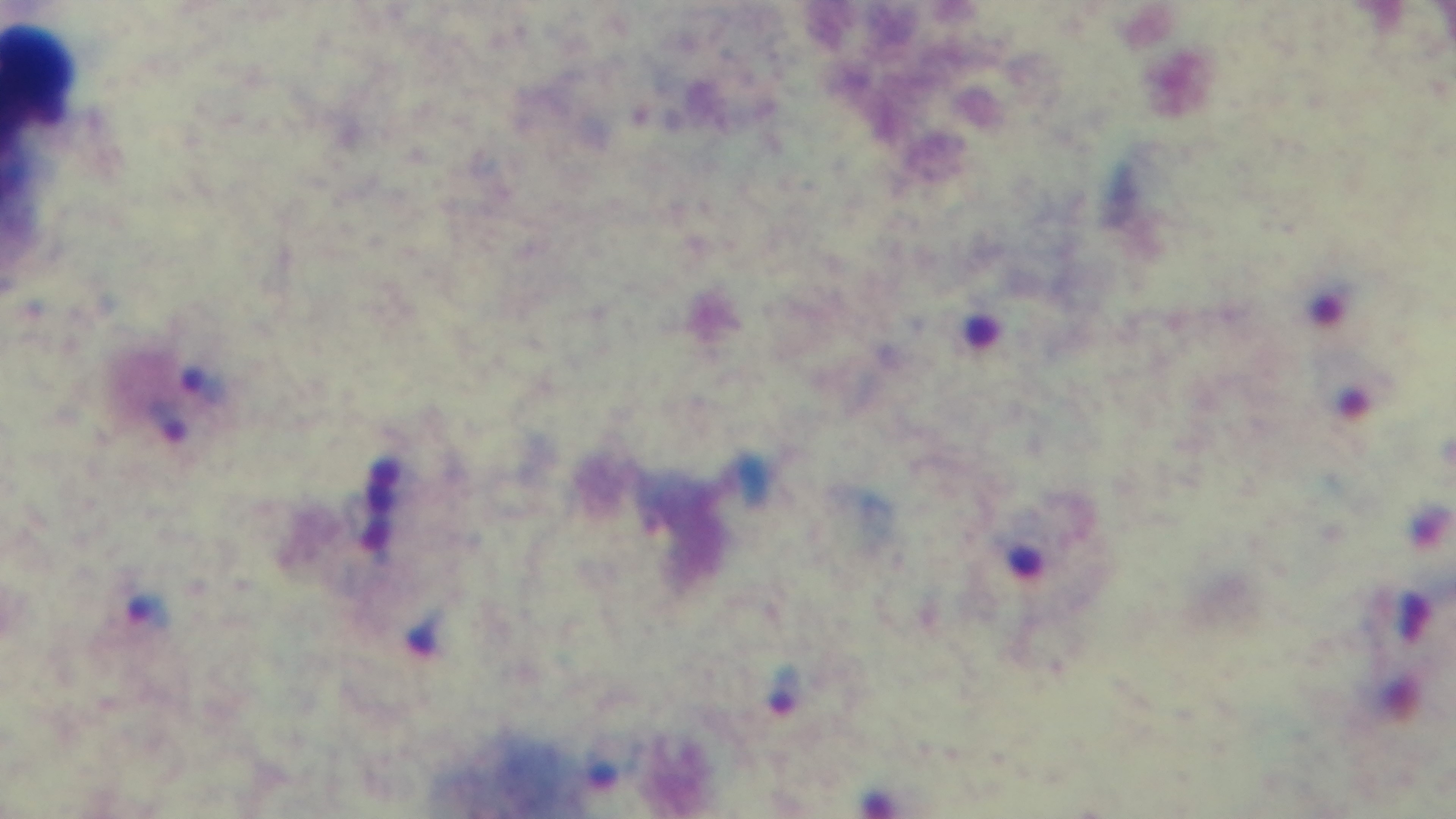

objective = 100x oil immersion
stain = Giemsa
malaria status = infected
preparation = thick smear
capture = mounted 4K digital camera
modality = light microscopy
field of view = single